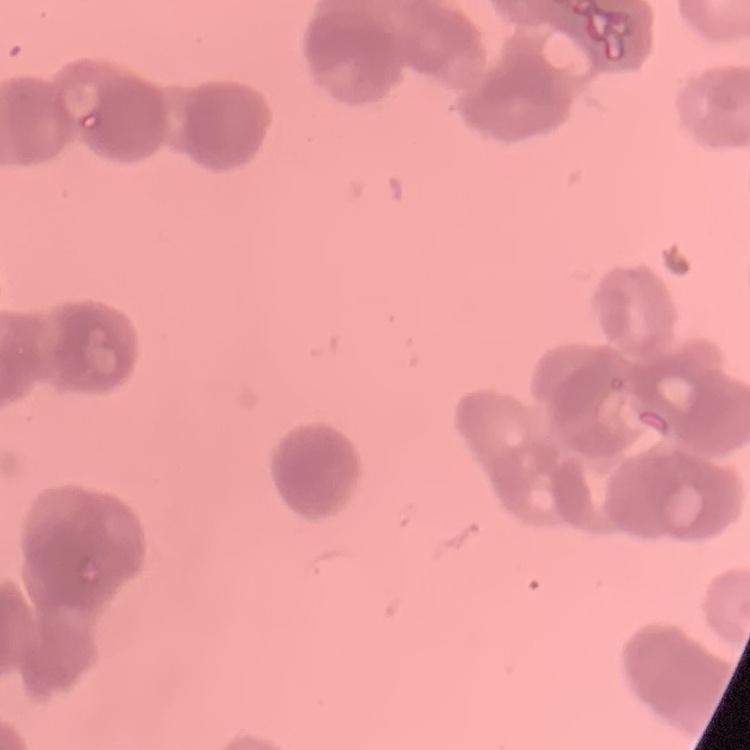

erythrocyte morphology = rouleaux formation
image type = square crop of a larger photomicrograph
stain = Field's or Giemsa
preparation = thin blood film